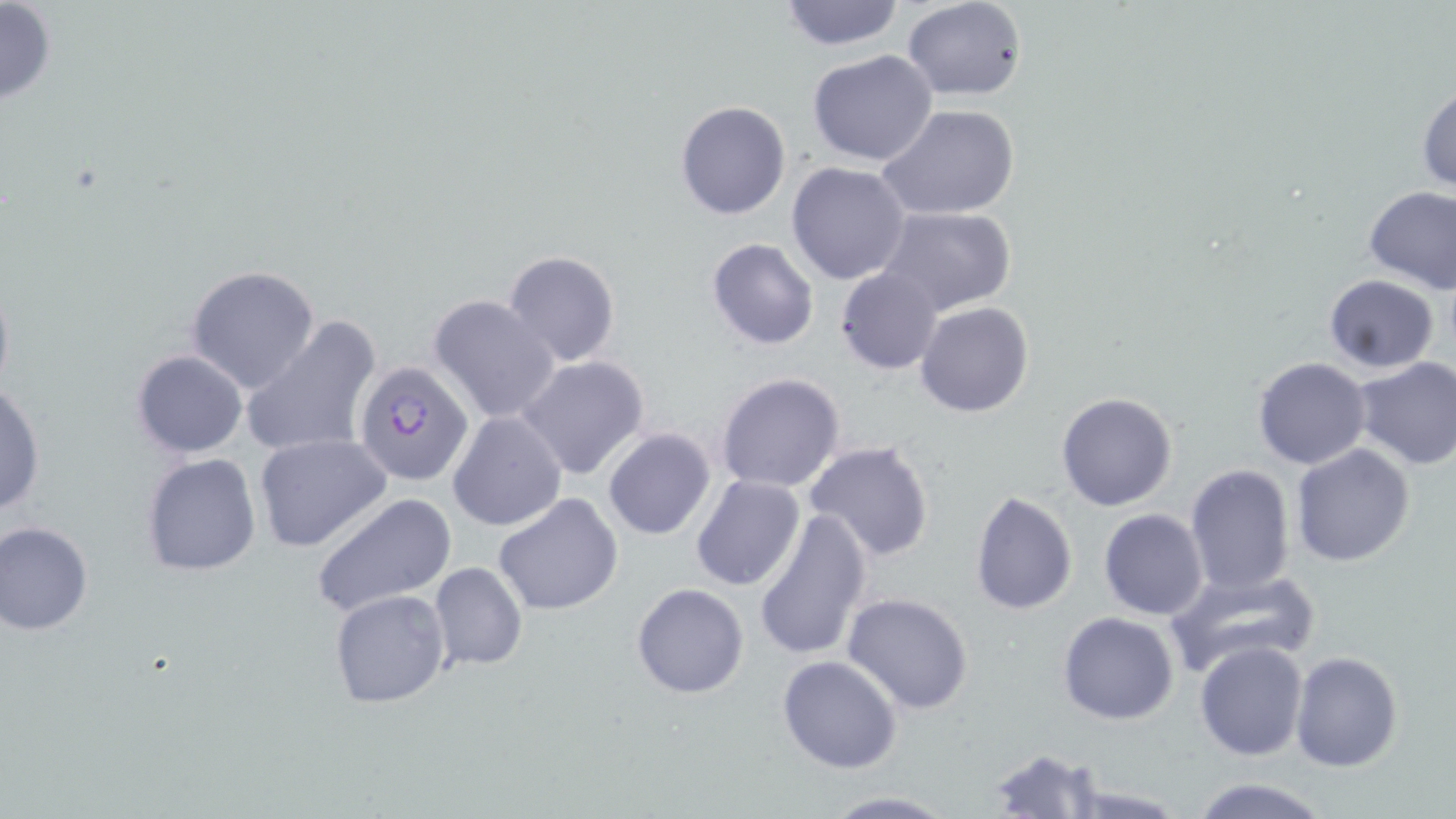

Summary:
  - Coordinate format: approximate bounding boxes as [x1, y1, x2, y2] in pixels
  - Uninfected red blood cell locations: [0, 0, 57, 109], [776, 0, 906, 51], [902, 0, 1026, 100], [807, 49, 939, 167], [1416, 81, 1456, 193], [675, 100, 791, 220], [879, 104, 1022, 220], [786, 162, 911, 284], [1363, 184, 1456, 294], [877, 206, 1017, 316], [706, 238, 819, 351], [501, 250, 620, 368], [185, 265, 323, 395], [836, 268, 944, 375], [1321, 274, 1439, 373], [429, 294, 560, 424], [916, 301, 1035, 418], [239, 315, 380, 461], [132, 349, 248, 458], [518, 356, 650, 480], [1252, 357, 1372, 470], [1352, 357, 1456, 470], [716, 372, 847, 494], [462, 379, 630, 509], [0, 383, 46, 520], [1056, 391, 1178, 512], [448, 411, 566, 532], [602, 427, 717, 541], [254, 433, 391, 553], [803, 440, 936, 564], [1290, 445, 1415, 568], [140, 454, 263, 576], [1185, 463, 1297, 597], [690, 474, 806, 592], [970, 489, 1078, 613], [311, 492, 457, 617], [493, 492, 624, 616], [753, 506, 872, 663], [1098, 508, 1209, 620], [1, 521, 93, 635], [429, 561, 528, 671], [1165, 566, 1320, 678], [631, 583, 749, 699], [330, 589, 452, 708], [843, 592, 975, 715], [1059, 612, 1179, 725], [1194, 642, 1307, 761], [1290, 650, 1401, 771], [777, 656, 904, 774], [985, 745, 1105, 817], [1186, 776, 1332, 818], [1055, 781, 1191, 818], [819, 792, 957, 818]
  - Plasmodium falciparum-infected red blood cell locations: [354, 361, 474, 486]
  - Slide-level diagnosis: Plasmodium falciparum
  - Magnification: 1000x
  - Modality: optical microscopy
  - Stain: May-Grünwald-Giemsa
  - Preparation: thin blood film
  - Field of view: one of a larger specimen
  - Image size: 1456×819 pixels